Assess this cell for malaria.
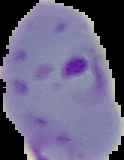

It is parasitized.

{
  "preparation": "thin blood smear",
  "image_size": "124×160 pixels",
  "image_type": "segmented cell region on a black background"
}